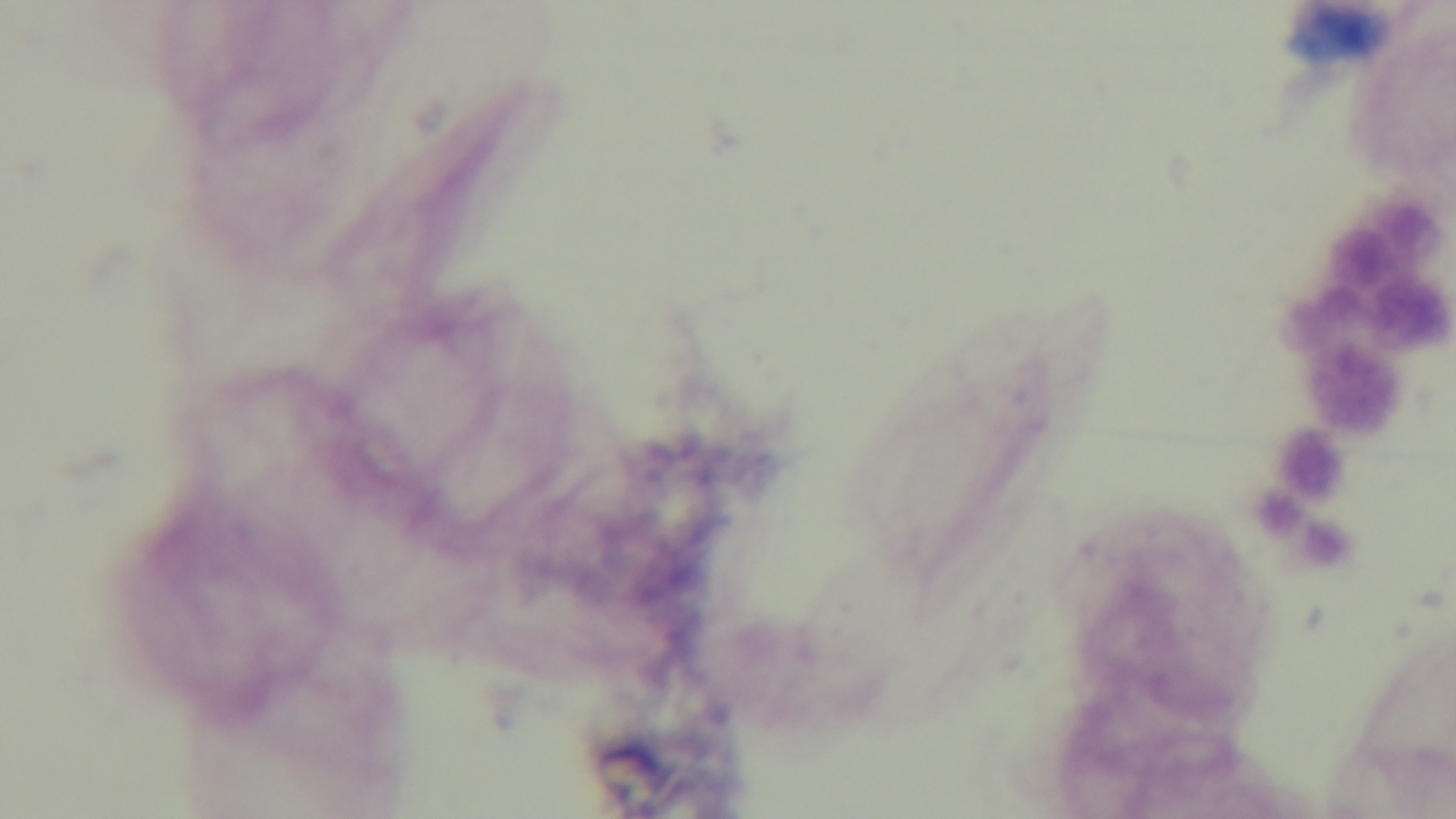
Summary:
  - Preparation: thick smear
  - Capture: mounted 4K digital camera
  - Modality: light microscopy
  - Field of view: single
  - Malaria status: negative
  - Objective: 100x oil immersion
  - Stain: Giemsa